Comment on the morphology of the erythrocytes.
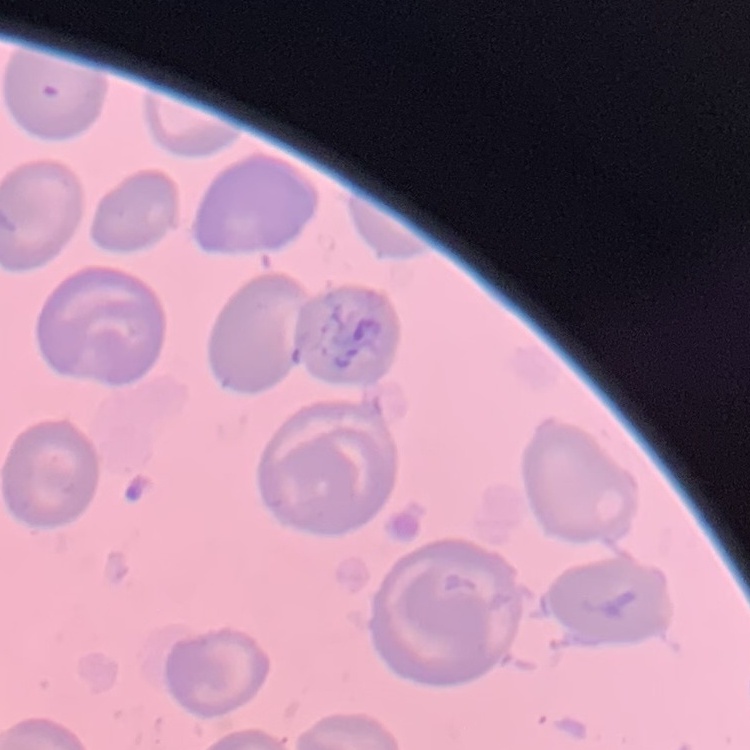
They show no rouleaux formation.

Summary:
  - Image type: square crop of a larger photomicrograph
  - Stain: Field's or Giemsa
  - Preparation: thin peripheral smear